Locate and identify every blood parasite.
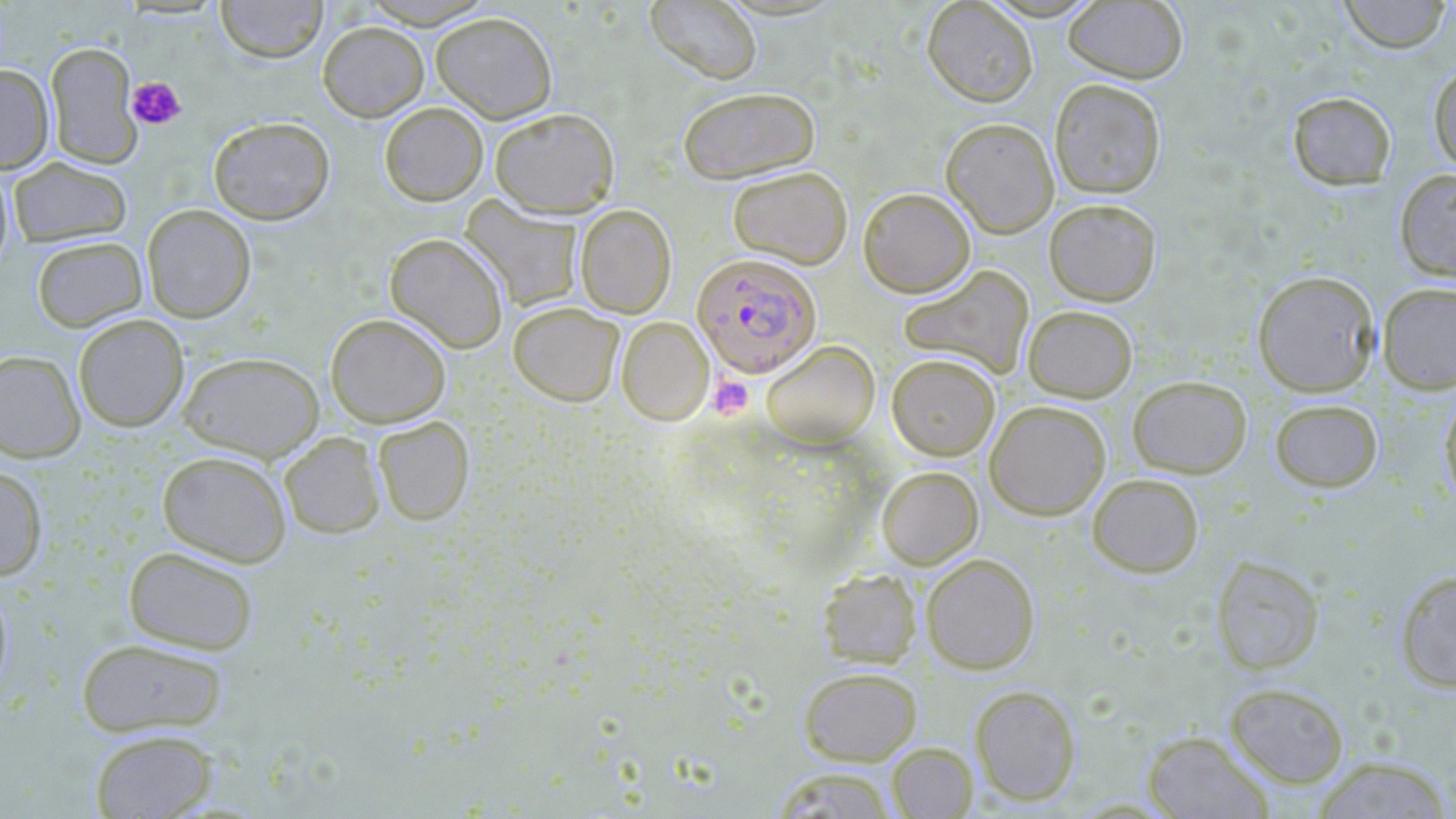

Approximate bounding boxes as [x1, y1, x2, y2] in pixels.
Plasmodium falciparum-infected red blood cells: [692, 253, 821, 377].
No Plasmodium ovale, Plasmodium malariae, Plasmodium vivax, Babesia divergens, or Trypanosoma brucei observed.

slide-level diagnosis = Plasmodium falciparum
field of view = single
modality = light microscopy
magnification = 1000x
platelet locations = approximate bounding boxes as [x1, y1, x2, y2] in pixels: [126, 76, 186, 130], [709, 376, 753, 419]
uninfected red blood cell locations = approximate bounding boxes as [x1, y1, x2, y2] in pixels: [215, 0, 328, 63], [358, 0, 495, 28], [646, 0, 762, 84], [922, 0, 1038, 106], [1337, 0, 1452, 53], [1063, 1, 1188, 83], [431, 12, 558, 123], [317, 21, 429, 121], [46, 41, 142, 168], [1428, 63, 1456, 174], [0, 64, 54, 174], [1049, 78, 1166, 198], [677, 86, 819, 183], [1287, 91, 1396, 190], [380, 102, 488, 205], [489, 107, 620, 217], [208, 117, 334, 224], [940, 117, 1059, 237], [8, 157, 132, 248], [0, 163, 14, 271], [727, 166, 852, 269], [1394, 169, 1456, 282], [858, 187, 975, 297], [460, 197, 583, 312], [1044, 198, 1161, 306], [142, 204, 256, 322], [575, 204, 677, 318], [385, 234, 509, 353], [32, 236, 147, 332], [898, 265, 1034, 380], [1252, 270, 1380, 396], [1377, 282, 1456, 394], [508, 302, 624, 406], [1023, 305, 1137, 402], [325, 313, 451, 427], [73, 314, 189, 432], [617, 316, 714, 425], [761, 340, 880, 447], [0, 350, 85, 463], [178, 352, 324, 462], [887, 353, 1000, 460], [1127, 375, 1252, 478], [1439, 388, 1456, 508], [1269, 398, 1383, 492], [985, 400, 1110, 520], [373, 416, 474, 525], [279, 432, 385, 538], [157, 450, 292, 567], [0, 466, 48, 581], [877, 467, 982, 568], [1087, 473, 1204, 578], [123, 545, 259, 655], [921, 553, 1040, 674], [1211, 554, 1325, 675], [818, 567, 922, 668], [1395, 570, 1456, 693], [0, 577, 13, 704], [75, 637, 229, 738], [798, 666, 922, 766], [1225, 682, 1349, 788], [970, 684, 1081, 805], [89, 729, 218, 818], [1142, 731, 1274, 818], [886, 742, 977, 818], [1310, 755, 1454, 819], [771, 767, 898, 818]
preparation = thin blood film
image size = 1456×819 pixels
stain = May-Grünwald-Giemsa